Assess this cell for malaria.
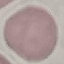
Uninfected.

Summary:
  - Capture: smartphone camera at the microscope eyepiece
  - Image type: automatically extracted cell patch, resized to 64 × 64 pixels
  - Stain: Giemsa
  - Preparation: thin blood smear